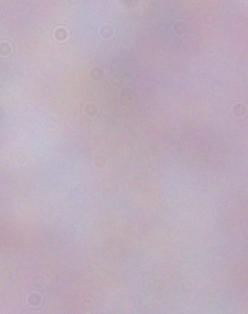
{
  "magnification": "1000x",
  "modality": "photomicrograph",
  "identification": "trypanosome"
}